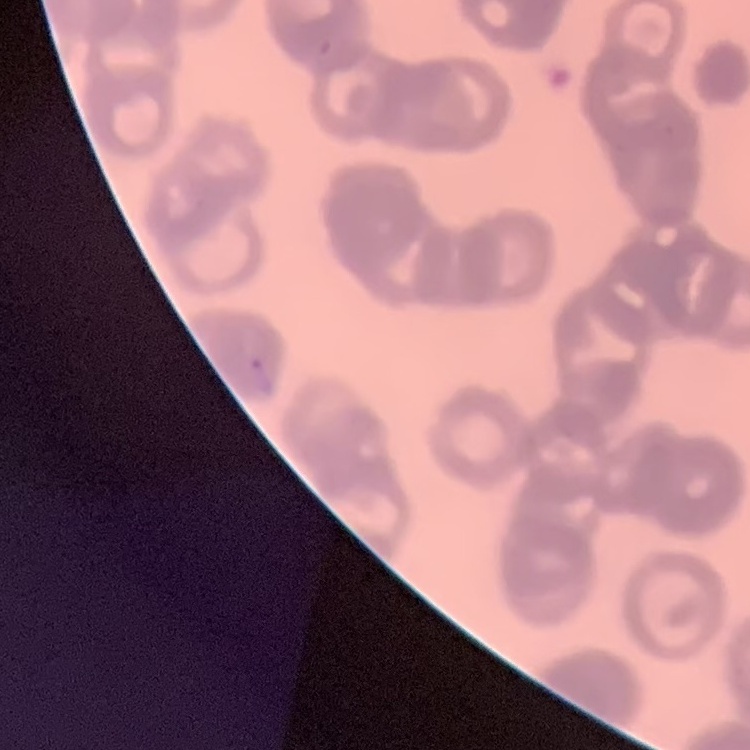

The red blood cells exhibit rouleaux formation. One tile cut from a larger photomicrograph. Stained with either Field's or Giemsa. Thin blood film.